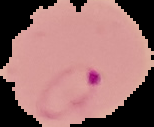

Summary:
  - Image size: 154×127 pixels
  - Image type: cell region segmented out of the field of view; surrounding area masked to black
  - Result: malaria parasites identified
  - Preparation: thin blood smear